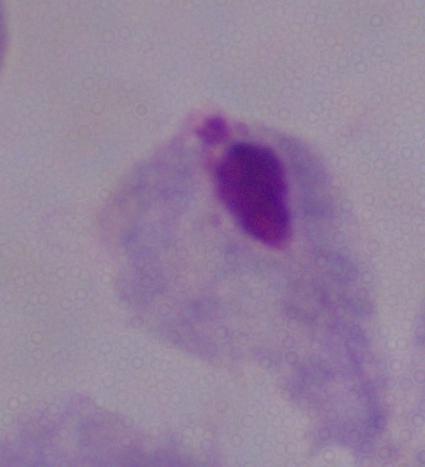

{
  "magnification": "1000x",
  "modality": "photomicrograph",
  "identification": "trichomonad"
}